Locate malaria parasites and leukocytes.
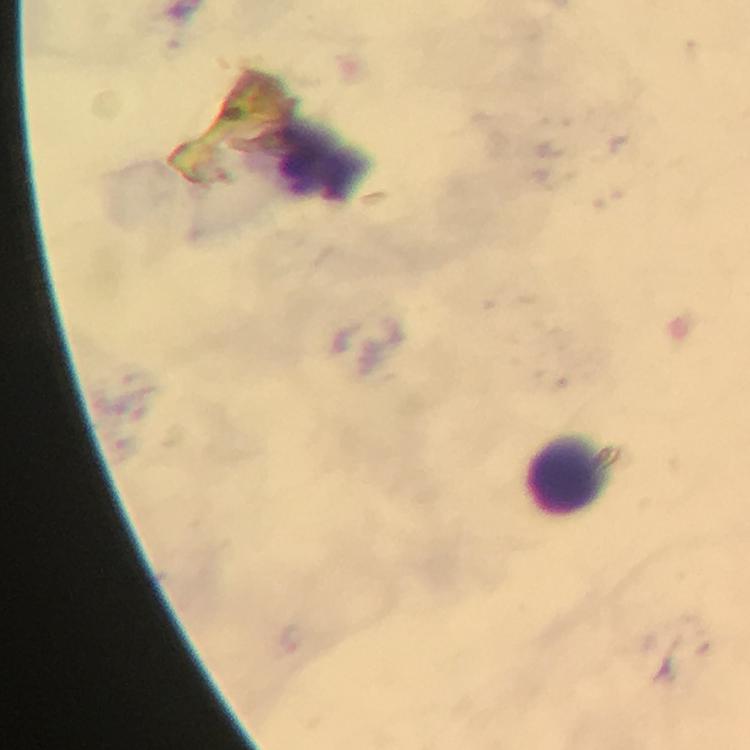

No malaria parasites detected.
Approximate object centers, in pixels from the top-left corner.
Leukocytes: (x=566, y=476).

Summary:
  - Stain: Giemsa
  - Cropped from: one field of view
  - Image size: 750×750 pixels
  - Capture: smartphone mounted on the microscope
  - Magnification: 100x
  - Immersion oil: used
  - Preparation: thick blood film
  - Context: from a malaria diagnostic workup